Outline each uninfected red blood cell.
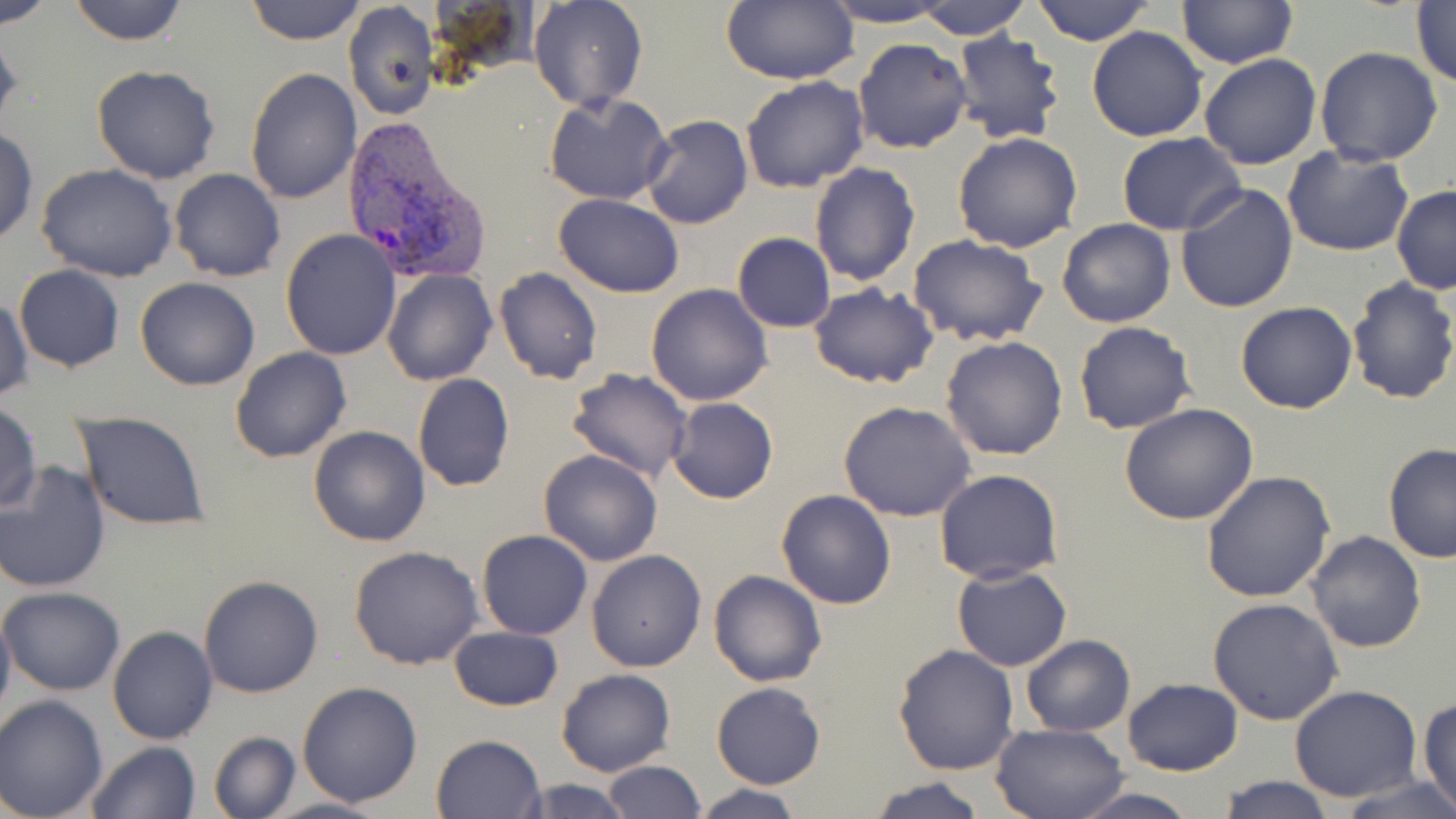

Approximate bounding boxes as (x1, y1, x2, y2) in pixels.
Uninfected red blood cells: (1, 0, 57, 28), (66, 0, 190, 45), (247, 0, 363, 45), (530, 0, 648, 111), (722, 0, 858, 85), (1031, 0, 1153, 46), (913, 1, 1035, 40), (1177, 1, 1296, 69), (1411, 1, 1456, 88), (817, 2, 955, 27), (342, 4, 436, 121), (1088, 26, 1206, 142), (0, 27, 24, 134), (953, 29, 1065, 145), (853, 37, 972, 154), (1092, 39, 1313, 154), (1314, 46, 1444, 166), (1199, 53, 1323, 169), (91, 64, 221, 184), (245, 68, 360, 204), (740, 75, 870, 192), (543, 93, 672, 206), (640, 113, 754, 230), (0, 125, 37, 248), (952, 132, 1084, 255), (1117, 133, 1245, 235), (1283, 146, 1416, 257), (809, 161, 919, 285), (36, 164, 179, 282), (169, 168, 286, 281), (1175, 183, 1299, 314), (1391, 184, 1456, 295), (552, 192, 685, 297), (1057, 218, 1175, 328), (280, 228, 401, 360), (732, 232, 836, 332), (905, 235, 1048, 348), (14, 264, 124, 370), (495, 267, 604, 386), (382, 269, 496, 386), (135, 277, 260, 391), (1344, 277, 1456, 404), (808, 282, 939, 388), (647, 283, 774, 405), (1, 294, 31, 404), (1235, 301, 1357, 415), (1075, 322, 1197, 435), (941, 335, 1070, 460), (229, 347, 351, 464), (566, 367, 693, 480), (412, 374, 514, 492), (667, 396, 778, 505), (838, 401, 977, 521), (0, 403, 43, 513), (1118, 403, 1259, 525), (73, 413, 210, 530), (308, 425, 431, 548), (1382, 444, 1456, 564), (538, 449, 665, 566), (0, 460, 114, 593), (935, 469, 1063, 584), (1200, 470, 1335, 603), (774, 490, 897, 610), (476, 529, 592, 640), (1306, 531, 1426, 652), (349, 545, 483, 670), (587, 549, 707, 672), (951, 564, 1072, 671), (708, 569, 827, 688), (198, 574, 325, 698), (1, 587, 126, 695), (1206, 597, 1343, 724), (0, 601, 15, 731), (449, 625, 563, 712), (107, 626, 218, 745), (1020, 634, 1134, 737), (893, 643, 1020, 774), (555, 668, 676, 777), (1123, 679, 1242, 776), (296, 681, 423, 808), (712, 681, 826, 788), (1289, 684, 1422, 802), (0, 694, 109, 819), (1418, 697, 1456, 816), (991, 721, 1131, 819), (210, 731, 299, 817), (431, 734, 546, 819), (84, 741, 200, 819), (604, 759, 705, 818), (866, 776, 987, 819), (1217, 776, 1337, 818), (1342, 777, 1455, 817), (512, 778, 639, 818), (690, 783, 804, 819), (1069, 788, 1203, 819), (261, 796, 393, 819).

Plasmodium vivax-infected red blood cell locations: (344, 117, 494, 285). Slide-level diagnosis: Plasmodium vivax. Optical microscopy. Single field of view. Image is 1456×819 pixels. Thin blood smear. Captured at 1000x magnification. May-Grünwald-Giemsa-stained preparation.